Describe the morphology of the red blood cells.
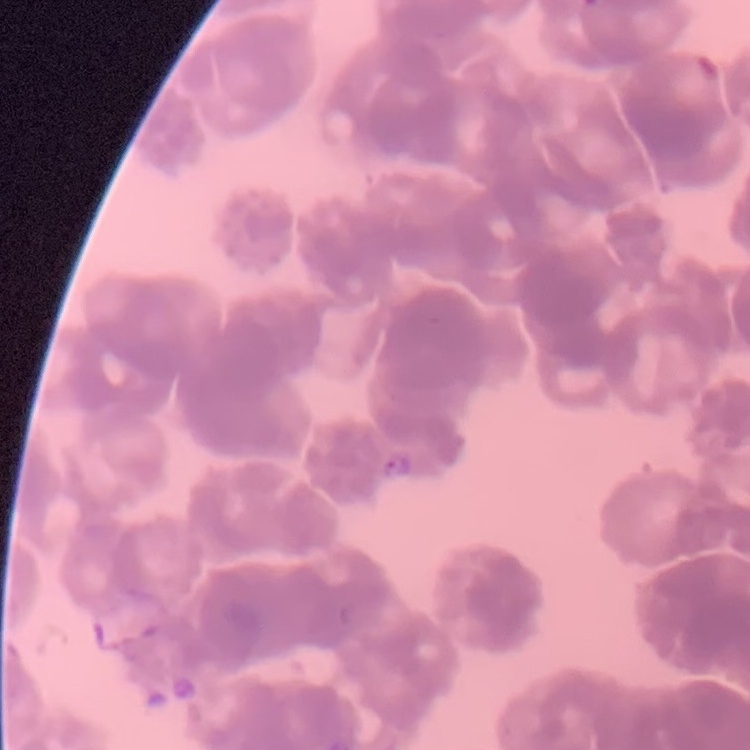

Rouleaux formation.

image_type: square crop of a larger photomicrograph
preparation: thin blood film
stain: Field's or Giemsa